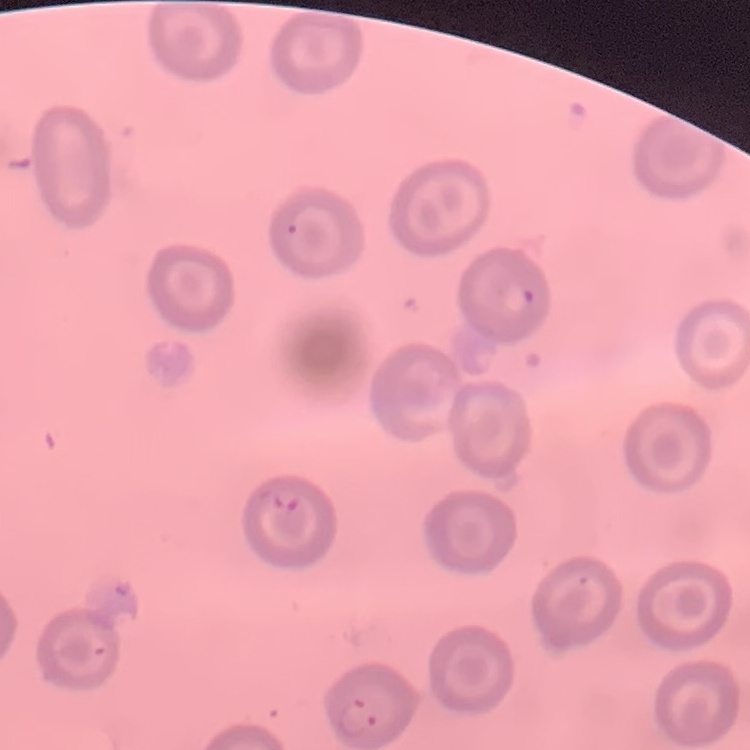
The red blood cells show no rouleaux formation. Thin peripheral smear. Square crop of a larger photomicrograph. Stained with either Field's or Giemsa.